Identify the cell.
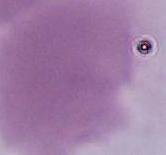
This is an erythrocyte.

magnification: 1000x
modality: photomicrograph